Assess the morphology of the red blood cells.
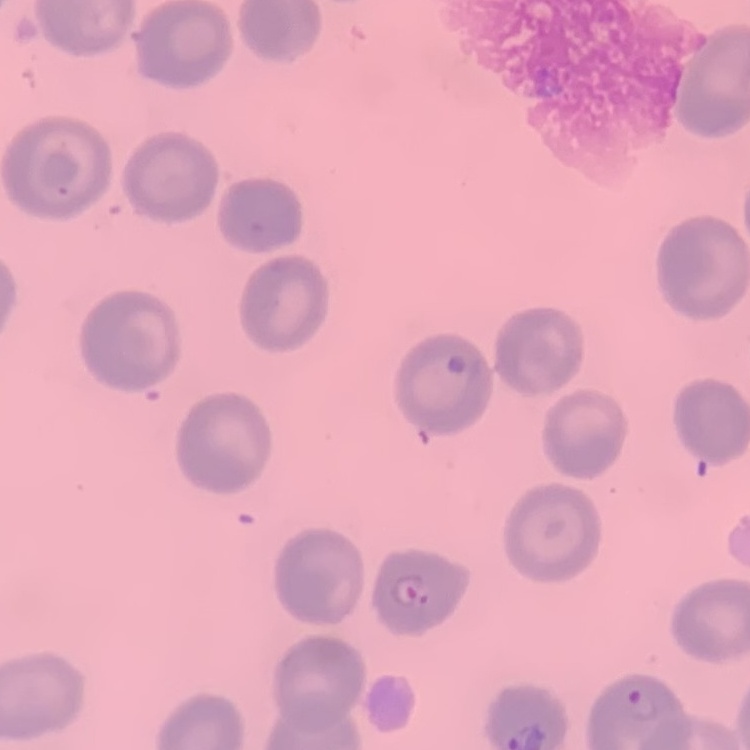
They show no rouleaux formation.

{
  "stain": "Field's or Giemsa",
  "image_type": "one tile cut from a larger photomicrograph",
  "preparation": "thin blood smear"
}